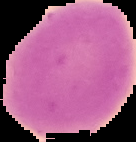

image_type: cell region segmented out of the field of view; surrounding area masked to black
preparation: thin blood smear
image_size: 136×142 pixels
result: negative for malaria parasites